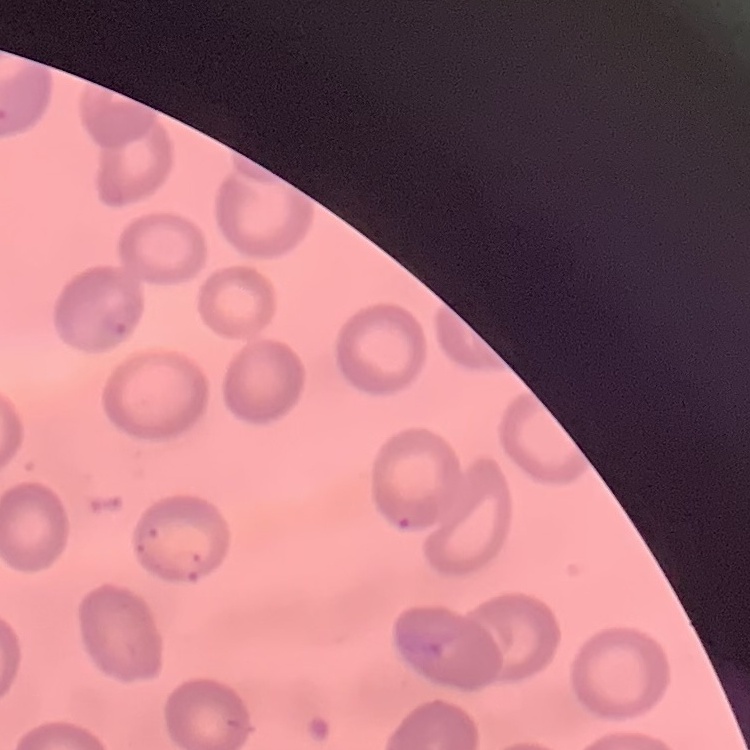

erythrocyte morphology = no rouleaux formation
stain = Field's or Giemsa
image type = one tile cut from a larger photomicrograph
preparation = thin blood film